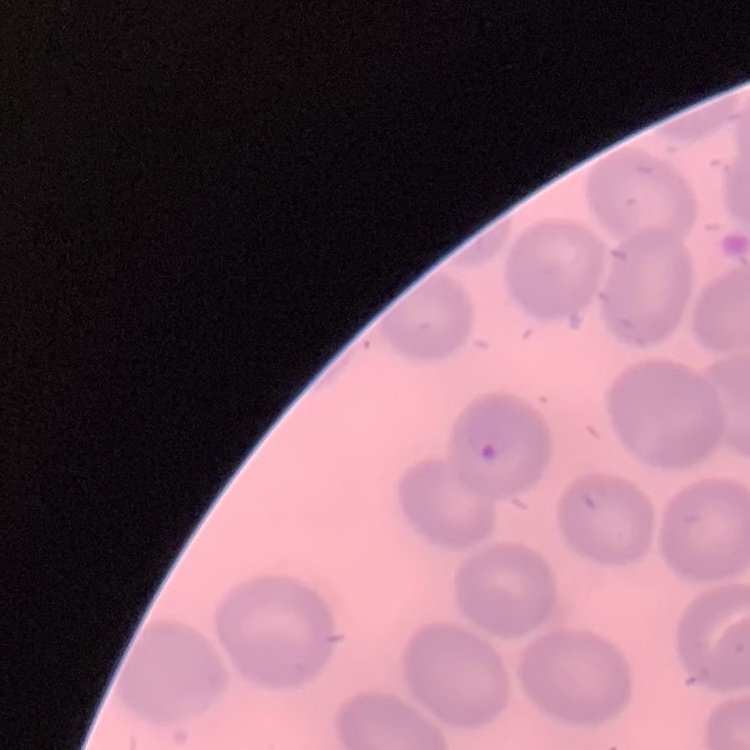
erythrocyte morphology = no rouleaux formation
stain = Field's or Giemsa
image type = one tile cut from a larger photomicrograph
preparation = thin blood smear